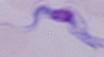

Summary:
  - Modality: micrograph
  - Magnification: 1000x
  - Identification: trypanosome